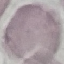

Result: negative for malaria parasites. Giemsa stain. Cell patch, automatically extracted from a larger field of view and resized to 64 × 64 pixels. Photographed with a smartphone camera at the microscope eyepiece. Thin smear of blood.